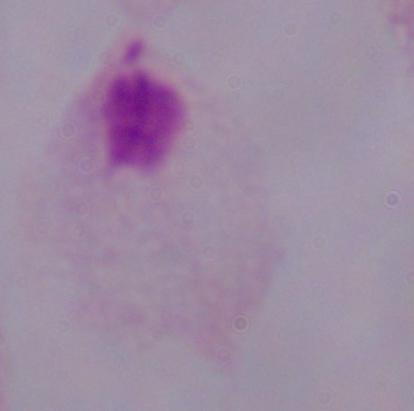 Micrograph. 1000x magnification. A trichomonad is seen.